Identify the blood parasite species.
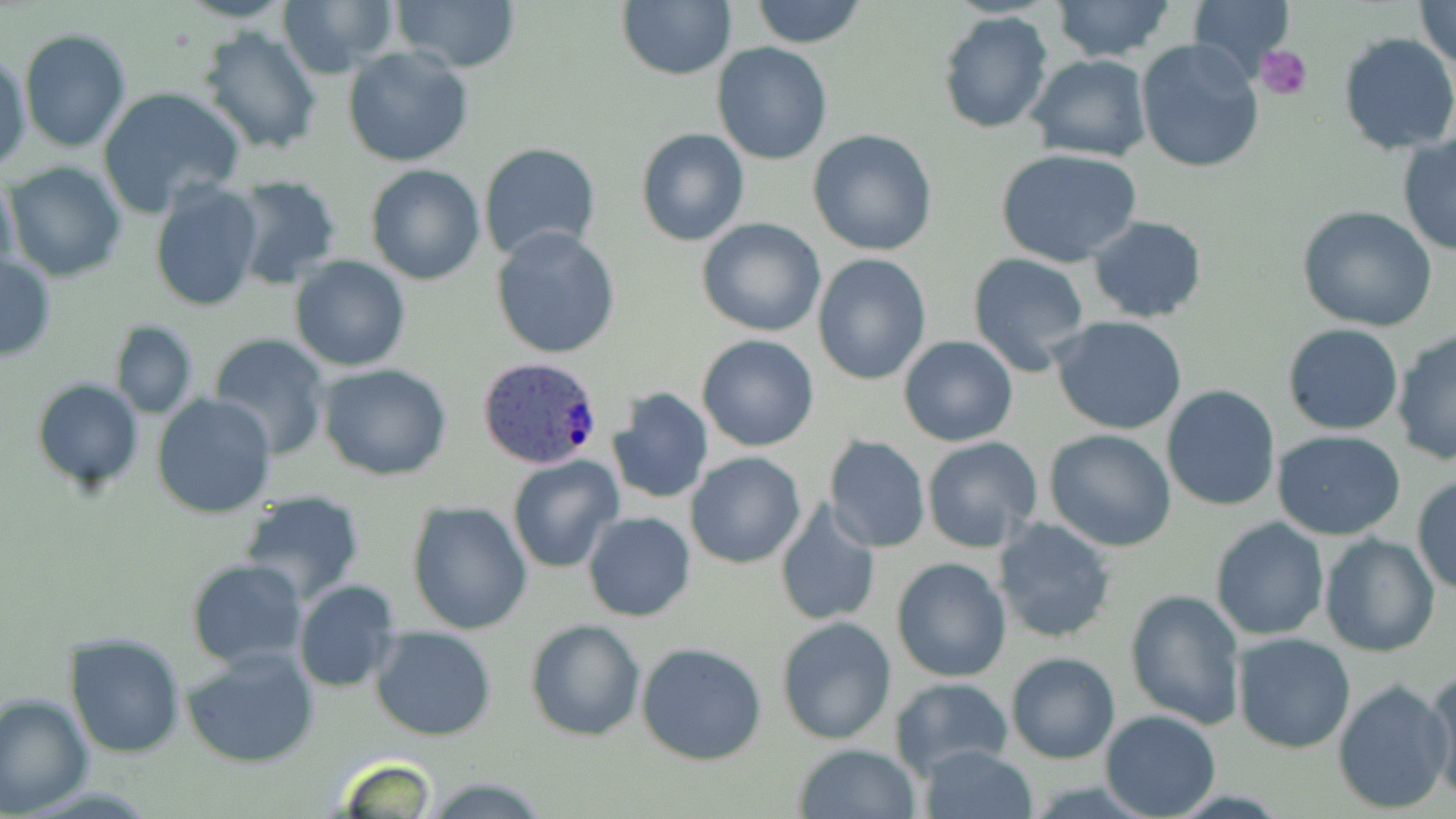

Plasmodium ovale.

Summary:
  - Coordinate format: approximate bounding boxes as [x1, y1, x2, y2] in pixels
  - Platelet locations: [1255, 45, 1312, 101]
  - Uninfected red blood cell locations: [172, 0, 296, 24], [391, 0, 519, 71], [749, 0, 869, 49], [1189, 0, 1298, 73], [1415, 0, 1456, 75], [279, 1, 397, 77], [1052, 1, 1174, 62], [617, 2, 736, 80], [937, 11, 1053, 134], [20, 28, 131, 152], [199, 29, 323, 155], [1338, 34, 1456, 155], [1135, 38, 1265, 176], [712, 43, 833, 165], [343, 47, 475, 168], [1, 49, 30, 173], [1026, 54, 1150, 162], [99, 86, 246, 219], [634, 126, 749, 247], [807, 129, 938, 256], [1398, 134, 1456, 256], [477, 141, 601, 261], [995, 148, 1142, 267], [365, 155, 601, 275], [3, 161, 127, 282], [366, 165, 485, 284], [0, 171, 21, 294], [230, 175, 343, 288], [149, 181, 265, 314], [1296, 206, 1439, 333], [1087, 214, 1208, 322], [696, 219, 826, 336], [490, 227, 623, 359], [967, 252, 1091, 376], [811, 254, 932, 386], [0, 255, 57, 363], [290, 255, 410, 372], [1049, 316, 1189, 436], [109, 321, 198, 419], [1281, 324, 1404, 435], [1391, 329, 1456, 466], [207, 334, 330, 461], [697, 335, 820, 452], [899, 336, 1017, 447], [318, 364, 454, 481], [32, 380, 143, 491], [1161, 384, 1281, 511], [608, 386, 714, 505], [151, 394, 276, 518], [1045, 429, 1177, 551], [1272, 430, 1406, 540], [824, 436, 931, 554], [921, 436, 1043, 552], [685, 453, 806, 569], [507, 456, 622, 573], [1411, 473, 1456, 596], [239, 488, 366, 605], [405, 500, 532, 634], [772, 500, 882, 628], [582, 511, 696, 622], [1209, 516, 1329, 641], [991, 517, 1117, 646], [1318, 533, 1440, 659], [891, 556, 1012, 681], [185, 559, 306, 671], [294, 580, 404, 694], [1125, 588, 1248, 729], [775, 616, 897, 745], [524, 618, 646, 742], [369, 626, 497, 741], [1231, 632, 1358, 753], [64, 633, 188, 757], [636, 642, 769, 766], [183, 646, 319, 769], [1005, 652, 1120, 765], [1426, 666, 1456, 802], [889, 676, 1014, 778], [1331, 679, 1453, 815], [0, 691, 93, 817], [1098, 710, 1221, 819], [793, 744, 920, 819], [914, 744, 1037, 819], [333, 752, 441, 818], [419, 777, 554, 816]
  - Plasmodium ovale-infected red blood cell locations: [475, 357, 605, 471]
  - Field of view: single
  - Image size: 1456×819 pixels
  - Stain: May-Grünwald-Giemsa
  - Modality: light microscopy
  - Preparation: thin blood film
  - Magnification: 1000x